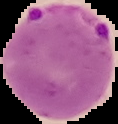 Image is 118×124 pixels. From a thin blood film. Segmented cell region on a black background. Malaria status: parasitized.